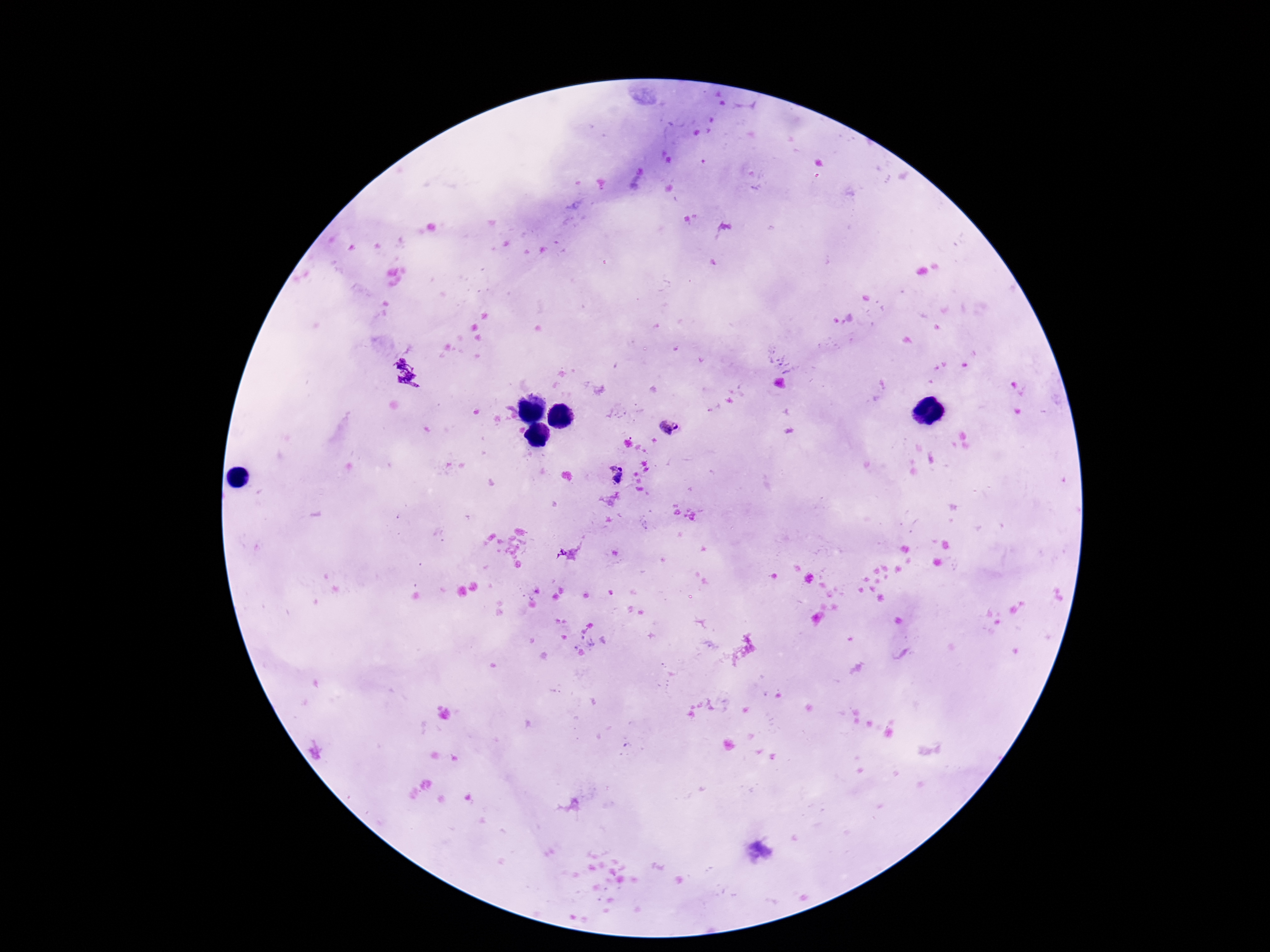
capture = smartphone camera through the microscope eyepiece
magnification = 100x
image size = 1270×952 pixels
preparation = thick blood film
field of view = single
Plasmodium parasite locations = approximate centers as {x, y} in pixels: {669, 427}, {615, 475}
stain = Giemsa
patient malaria status = positive